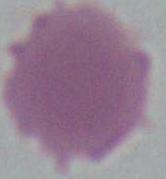

{
  "magnification": "1000x",
  "modality": "photomicrograph",
  "identification": "red blood cell"
}